Classify this cell by malaria status.
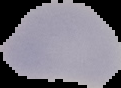
It is uninfected.

From a thin blood film. Image is 121×88 pixels. The area outside the segmented cell region is set to black.